Outline each blood parasite and name the species.
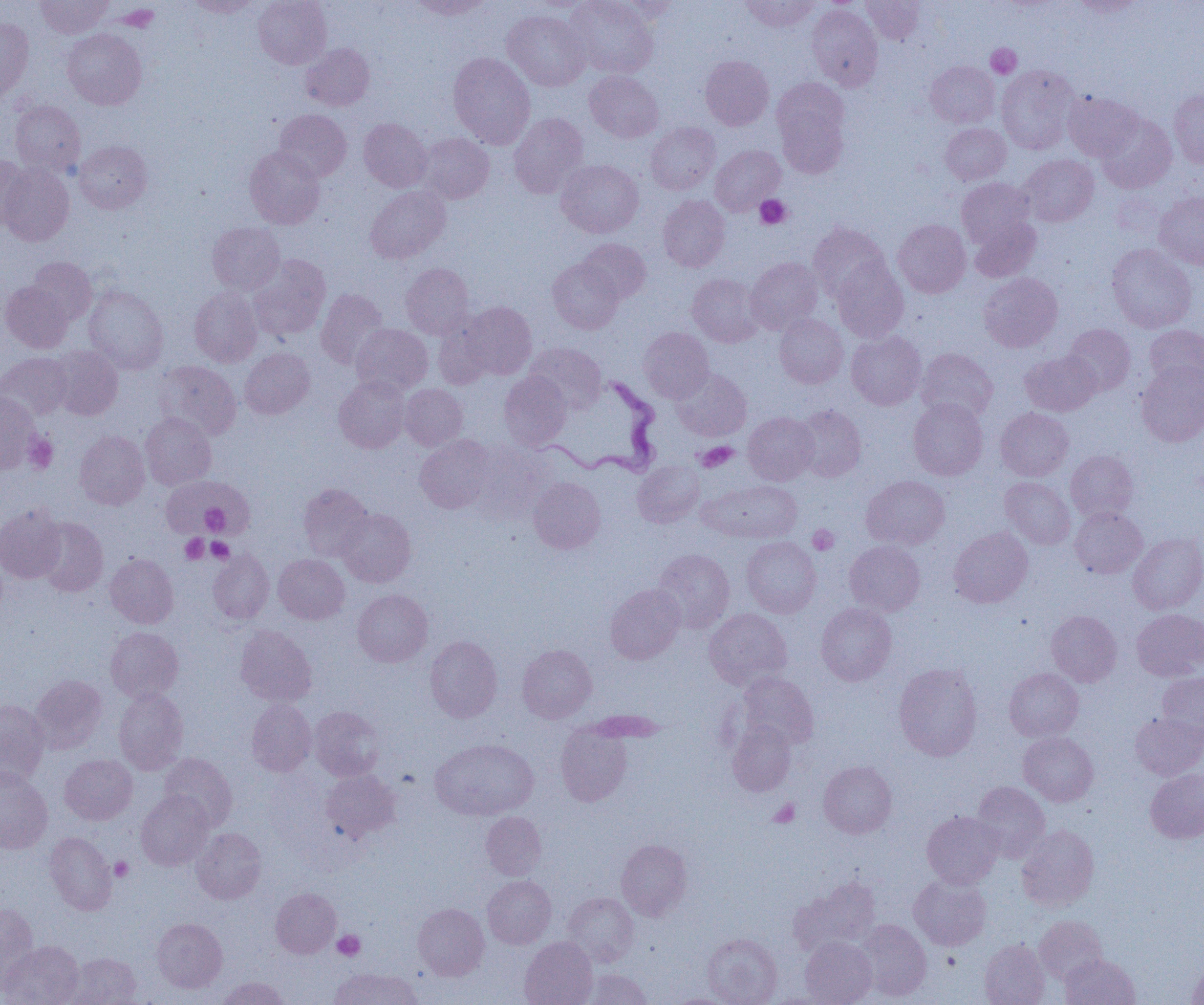

Approximate bounding boxes as named x1/y1/x2/y2 corners in pixels.
Trypanosoma brucei: (x1=536, y1=376, x2=662, y2=477).
No Plasmodium falciparum, Plasmodium ovale, Plasmodium malariae, Plasmodium vivax, or Babesia divergens observed.

Uninfected red blood cell locations: (x1=36, y1=0, x2=113, y2=38), (x1=184, y1=0, x2=263, y2=17), (x1=254, y1=0, x2=332, y2=69), (x1=408, y1=0, x2=494, y2=19), (x1=565, y1=0, x2=658, y2=78), (x1=606, y1=0, x2=680, y2=24), (x1=741, y1=0, x2=820, y2=32), (x1=861, y1=0, x2=925, y2=45), (x1=1072, y1=0, x2=1146, y2=18), (x1=806, y1=4, x2=883, y2=91), (x1=502, y1=9, x2=590, y2=91), (x1=0, y1=18, x2=33, y2=104), (x1=63, y1=28, x2=146, y2=109), (x1=301, y1=43, x2=375, y2=111), (x1=448, y1=52, x2=535, y2=148), (x1=701, y1=55, x2=774, y2=130), (x1=925, y1=60, x2=999, y2=128), (x1=996, y1=66, x2=1079, y2=153), (x1=585, y1=71, x2=664, y2=143), (x1=771, y1=77, x2=851, y2=171), (x1=1169, y1=89, x2=1204, y2=168), (x1=1063, y1=92, x2=1142, y2=161), (x1=10, y1=100, x2=86, y2=177), (x1=274, y1=109, x2=351, y2=181), (x1=1096, y1=112, x2=1176, y2=193), (x1=509, y1=113, x2=588, y2=198), (x1=358, y1=118, x2=432, y2=192), (x1=645, y1=122, x2=720, y2=195), (x1=940, y1=123, x2=1011, y2=184), (x1=415, y1=133, x2=494, y2=204), (x1=75, y1=141, x2=152, y2=213), (x1=710, y1=145, x2=785, y2=215), (x1=245, y1=146, x2=325, y2=228), (x1=1019, y1=154, x2=1098, y2=226), (x1=0, y1=156, x2=30, y2=229), (x1=556, y1=159, x2=644, y2=238), (x1=0, y1=164, x2=73, y2=246), (x1=957, y1=178, x2=1036, y2=248), (x1=365, y1=186, x2=450, y2=263), (x1=1154, y1=191, x2=1204, y2=270), (x1=658, y1=195, x2=730, y2=271), (x1=968, y1=215, x2=1041, y2=282), (x1=893, y1=219, x2=971, y2=298), (x1=207, y1=222, x2=285, y2=294), (x1=808, y1=222, x2=890, y2=302), (x1=578, y1=238, x2=651, y2=303), (x1=1107, y1=243, x2=1197, y2=333), (x1=248, y1=253, x2=331, y2=340), (x1=27, y1=257, x2=96, y2=324), (x1=746, y1=257, x2=823, y2=334), (x1=547, y1=258, x2=623, y2=334), (x1=831, y1=259, x2=909, y2=342), (x1=400, y1=263, x2=474, y2=338), (x1=979, y1=272, x2=1063, y2=352), (x1=687, y1=273, x2=764, y2=347), (x1=1, y1=281, x2=73, y2=352), (x1=84, y1=286, x2=168, y2=374), (x1=189, y1=286, x2=262, y2=367), (x1=315, y1=289, x2=388, y2=368), (x1=460, y1=302, x2=537, y2=380), (x1=774, y1=314, x2=848, y2=388), (x1=433, y1=317, x2=495, y2=389), (x1=351, y1=324, x2=432, y2=396), (x1=1063, y1=324, x2=1135, y2=395), (x1=1144, y1=325, x2=1204, y2=394), (x1=639, y1=327, x2=714, y2=401), (x1=846, y1=330, x2=926, y2=410), (x1=525, y1=342, x2=606, y2=413), (x1=48, y1=345, x2=123, y2=420), (x1=240, y1=348, x2=314, y2=418), (x1=916, y1=348, x2=998, y2=423), (x1=1020, y1=350, x2=1100, y2=416), (x1=0, y1=352, x2=72, y2=420), (x1=155, y1=360, x2=241, y2=440), (x1=1136, y1=362, x2=1204, y2=446), (x1=672, y1=368, x2=752, y2=441), (x1=498, y1=371, x2=571, y2=450), (x1=334, y1=376, x2=410, y2=452), (x1=399, y1=383, x2=468, y2=450), (x1=0, y1=392, x2=40, y2=473), (x1=908, y1=397, x2=988, y2=480), (x1=792, y1=405, x2=866, y2=482), (x1=995, y1=408, x2=1073, y2=481), (x1=743, y1=412, x2=819, y2=485), (x1=140, y1=413, x2=216, y2=490), (x1=75, y1=431, x2=150, y2=509), (x1=415, y1=435, x2=497, y2=513), (x1=467, y1=440, x2=555, y2=520), (x1=1066, y1=450, x2=1138, y2=522), (x1=633, y1=460, x2=704, y2=527), (x1=160, y1=475, x2=249, y2=537), (x1=862, y1=475, x2=949, y2=549), (x1=529, y1=477, x2=605, y2=553), (x1=1000, y1=477, x2=1075, y2=549), (x1=700, y1=479, x2=802, y2=543), (x1=298, y1=483, x2=372, y2=561), (x1=0, y1=503, x2=66, y2=583), (x1=1070, y1=507, x2=1147, y2=578), (x1=337, y1=508, x2=416, y2=587), (x1=36, y1=517, x2=108, y2=596), (x1=949, y1=528, x2=1033, y2=608), (x1=1128, y1=533, x2=1204, y2=614), (x1=742, y1=536, x2=821, y2=617), (x1=845, y1=540, x2=925, y2=615), (x1=652, y1=549, x2=734, y2=633), (x1=208, y1=550, x2=274, y2=623), (x1=105, y1=553, x2=179, y2=628), (x1=274, y1=554, x2=349, y2=624), (x1=605, y1=583, x2=685, y2=664), (x1=353, y1=589, x2=432, y2=667), (x1=816, y1=603, x2=896, y2=685), (x1=704, y1=608, x2=792, y2=690), (x1=1132, y1=609, x2=1204, y2=681), (x1=1046, y1=610, x2=1121, y2=686), (x1=235, y1=625, x2=317, y2=706), (x1=106, y1=627, x2=183, y2=703), (x1=425, y1=636, x2=502, y2=722), (x1=517, y1=644, x2=597, y2=722), (x1=894, y1=662, x2=982, y2=761), (x1=1004, y1=668, x2=1083, y2=741), (x1=737, y1=671, x2=818, y2=750), (x1=1157, y1=672, x2=1204, y2=740), (x1=30, y1=675, x2=107, y2=753), (x1=114, y1=688, x2=188, y2=774), (x1=246, y1=698, x2=316, y2=776), (x1=0, y1=700, x2=49, y2=785), (x1=310, y1=706, x2=385, y2=780), (x1=1130, y1=712, x2=1204, y2=779), (x1=727, y1=721, x2=796, y2=796), (x1=555, y1=724, x2=632, y2=806), (x1=1019, y1=732, x2=1099, y2=806), (x1=430, y1=738, x2=538, y2=820), (x1=159, y1=752, x2=237, y2=830), (x1=60, y1=754, x2=137, y2=824), (x1=819, y1=761, x2=897, y2=838), (x1=0, y1=768, x2=52, y2=854), (x1=1146, y1=768, x2=1204, y2=843), (x1=321, y1=769, x2=400, y2=843), (x1=971, y1=781, x2=1050, y2=861), (x1=136, y1=791, x2=214, y2=870), (x1=922, y1=811, x2=1004, y2=888), (x1=481, y1=812, x2=546, y2=880), (x1=1017, y1=825, x2=1099, y2=911), (x1=192, y1=828, x2=266, y2=904), (x1=45, y1=832, x2=116, y2=914), (x1=616, y1=839, x2=693, y2=920), (x1=908, y1=873, x2=991, y2=950), (x1=482, y1=875, x2=556, y2=948), (x1=788, y1=876, x2=880, y2=956), (x1=271, y1=888, x2=340, y2=958), (x1=562, y1=892, x2=638, y2=967), (x1=0, y1=903, x2=39, y2=989), (x1=413, y1=903, x2=489, y2=980), (x1=1034, y1=916, x2=1108, y2=984), (x1=152, y1=917, x2=227, y2=992), (x1=853, y1=919, x2=932, y2=1001), (x1=702, y1=933, x2=782, y2=1005), (x1=801, y1=936, x2=877, y2=1005), (x1=520, y1=937, x2=597, y2=1005), (x1=980, y1=939, x2=1049, y2=1005), (x1=1, y1=941, x2=84, y2=1005), (x1=64, y1=952, x2=141, y2=1005), (x1=1060, y1=954, x2=1140, y2=1005), (x1=1187, y1=958, x2=1204, y2=1004), (x1=329, y1=967, x2=423, y2=1005), (x1=579, y1=968, x2=653, y2=1005), (x1=217, y1=977, x2=290, y2=1004), (x1=764, y1=991, x2=842, y2=1004), (x1=667, y1=993, x2=736, y2=1005). Platelet locations: (x1=986, y1=43, x2=1021, y2=78), (x1=755, y1=195, x2=791, y2=229), (x1=23, y1=433, x2=58, y2=473), (x1=695, y1=441, x2=737, y2=472), (x1=201, y1=503, x2=228, y2=536), (x1=807, y1=525, x2=839, y2=554), (x1=181, y1=533, x2=208, y2=564), (x1=207, y1=538, x2=234, y2=563), (x1=769, y1=799, x2=800, y2=827), (x1=110, y1=857, x2=133, y2=881), (x1=333, y1=930, x2=364, y2=960). Slide-level diagnosis: Trypanosoma brucei. Light microscopy. 1000x magnification. Image is 1204×1005 pixels. One field of a larger specimen. Thin blood smear.